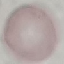

Summary:
  - Result: no malaria parasites seen
  - Image type: automatically extracted cell patch, resized to 64 × 64 pixels
  - Preparation: thin smear
  - Capture: smartphone camera at the microscope eyepiece
  - Stain: Giemsa